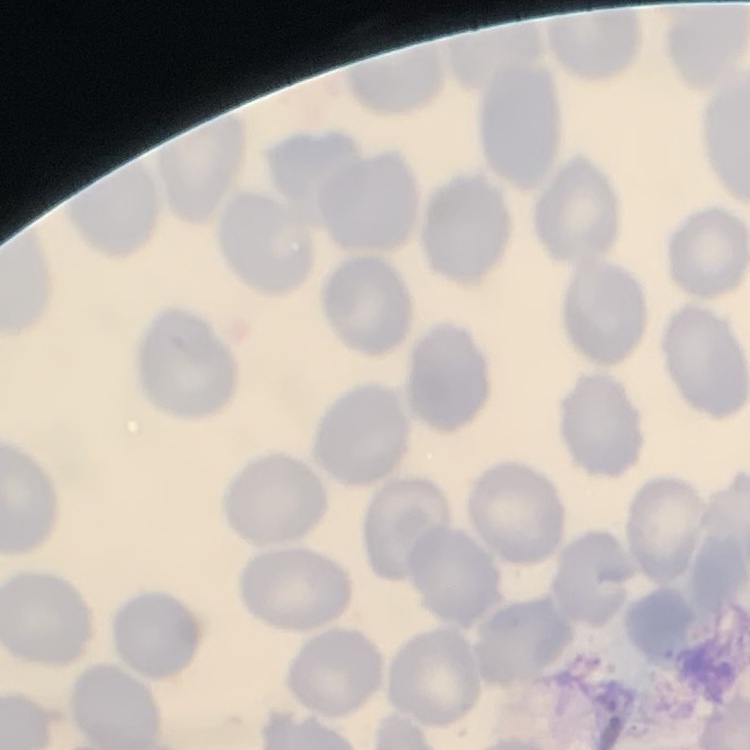

red_blood_cell_morphology: no rouleaux formation
image_type: square crop of a larger photomicrograph
stain: Field's or Giemsa
preparation: thin blood smear